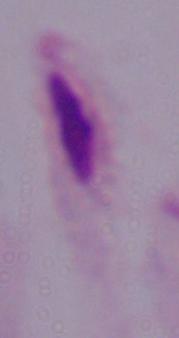

Summary:
  - Identification: trichomonad
  - Magnification: 1000x
  - Modality: photomicrograph